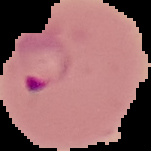

Image is 151×151 pixels. From a thin blood film. Cell region segmented out of the field of view; the surrounding area is masked to black. Malaria status: parasitized.